Identify the parasite.
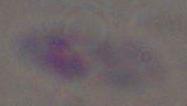

This is Toxoplasma gondii.

{
  "modality": "micrograph",
  "magnification": "1000x"
}